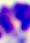
Summary:
  - Modality: photomicrograph
  - Magnification: 400x
  - Identification: leukocyte